Comment on the morphology of the red blood cells.
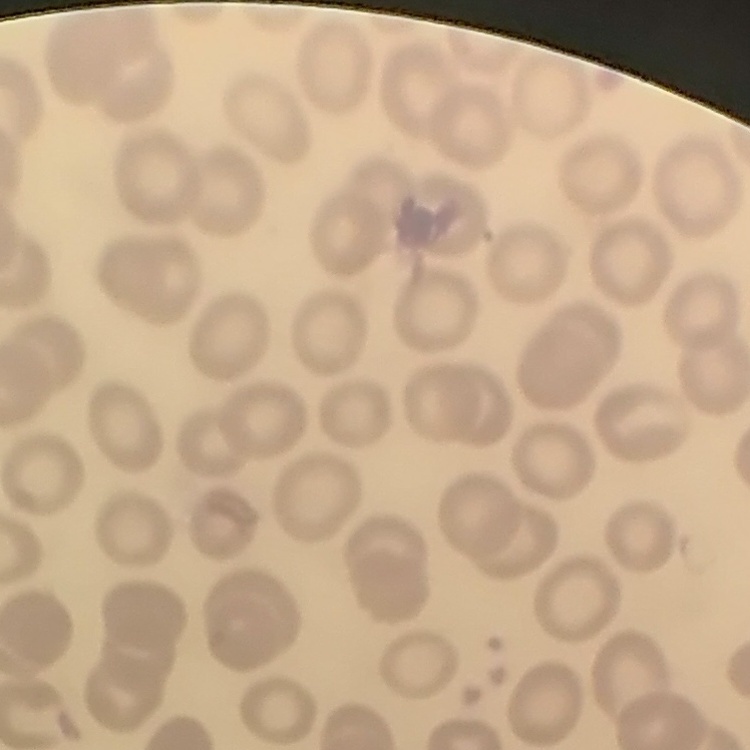

No rouleaux formation.

{
  "preparation": "thin peripheral smear",
  "stain": "Field's or Giemsa",
  "image_type": "square crop of a larger photomicrograph"
}